State which parasite is depicted.
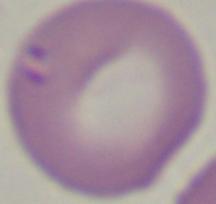
This is Babesia.

1000x magnification. Photomicrograph.